Outline each blood parasite and name the species.
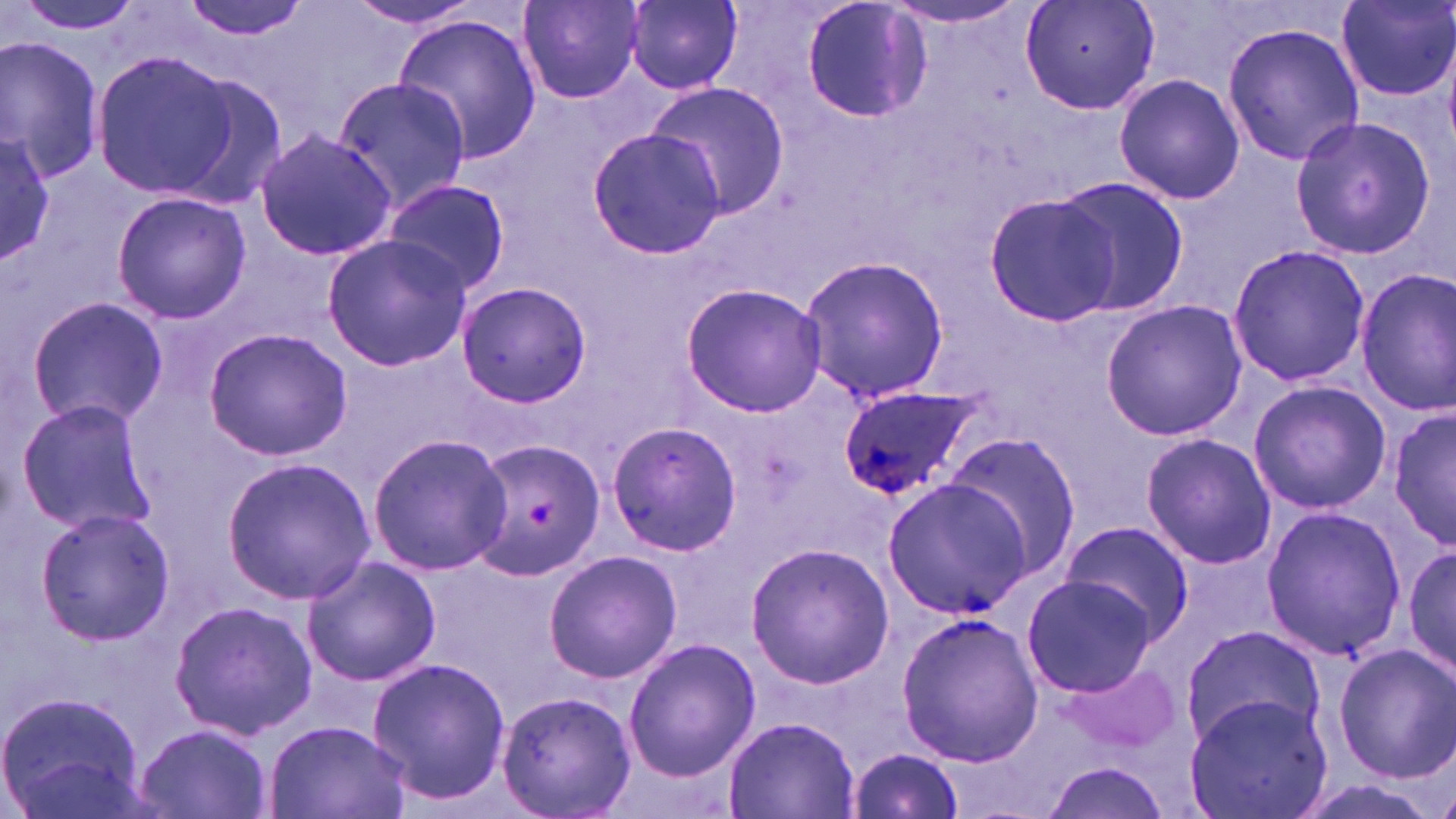

Approximate bounding boxes as (x1, y1, x2, y2) in pixels.
Plasmodium ovale-infected red blood cells: (835, 385, 978, 498).
No Plasmodium falciparum, Plasmodium malariae, Plasmodium vivax, Babesia divergens, or Trypanosoma brucei observed.

Platelet locations: (525, 501, 559, 528). Uninfected red blood cell locations: (12, 0, 150, 39), (179, 0, 311, 42), (626, 0, 743, 92), (884, 0, 1032, 29), (1020, 0, 1160, 117), (1337, 0, 1456, 103), (344, 1, 487, 30), (518, 1, 645, 105), (801, 2, 931, 123), (393, 16, 542, 163), (1221, 20, 1364, 166), (0, 37, 105, 181), (89, 47, 239, 200), (165, 71, 292, 213), (1113, 73, 1245, 206), (330, 74, 473, 215), (647, 86, 787, 218), (1288, 116, 1437, 258), (0, 126, 56, 269), (587, 126, 728, 260), (255, 128, 399, 263), (1052, 175, 1187, 314), (381, 179, 511, 295), (110, 191, 252, 324), (983, 193, 1120, 324), (321, 234, 473, 372), (1226, 242, 1370, 388), (798, 255, 951, 404), (1354, 269, 1456, 418), (680, 281, 828, 418), (456, 282, 591, 406), (24, 296, 168, 430), (1099, 296, 1247, 440), (201, 328, 353, 461), (1247, 380, 1391, 515), (16, 398, 158, 539), (1389, 406, 1455, 553), (606, 420, 741, 557), (1140, 432, 1278, 570), (366, 433, 513, 576), (942, 433, 1082, 577), (467, 438, 608, 582), (223, 456, 375, 604), (882, 479, 1033, 616), (1259, 505, 1409, 662), (32, 506, 178, 646), (1057, 520, 1195, 644), (1402, 539, 1455, 684), (745, 542, 894, 690), (543, 548, 684, 684), (300, 556, 442, 687), (1022, 573, 1159, 697), (169, 599, 317, 740), (897, 611, 1043, 767), (1179, 623, 1327, 749), (622, 638, 760, 780), (1333, 641, 1455, 784), (366, 657, 512, 805), (1056, 660, 1180, 757), (496, 687, 635, 819), (0, 690, 149, 819), (1183, 693, 1334, 819), (724, 714, 858, 818), (263, 718, 411, 819), (135, 724, 271, 819), (846, 747, 965, 818), (1037, 760, 1174, 819). Slide-level diagnosis: Plasmodium ovale. Thin blood film. Light microscopy. May-Grünwald-Giemsa stain. Image is 1456×819 pixels. Captured at 1000x magnification. One field of a larger specimen.